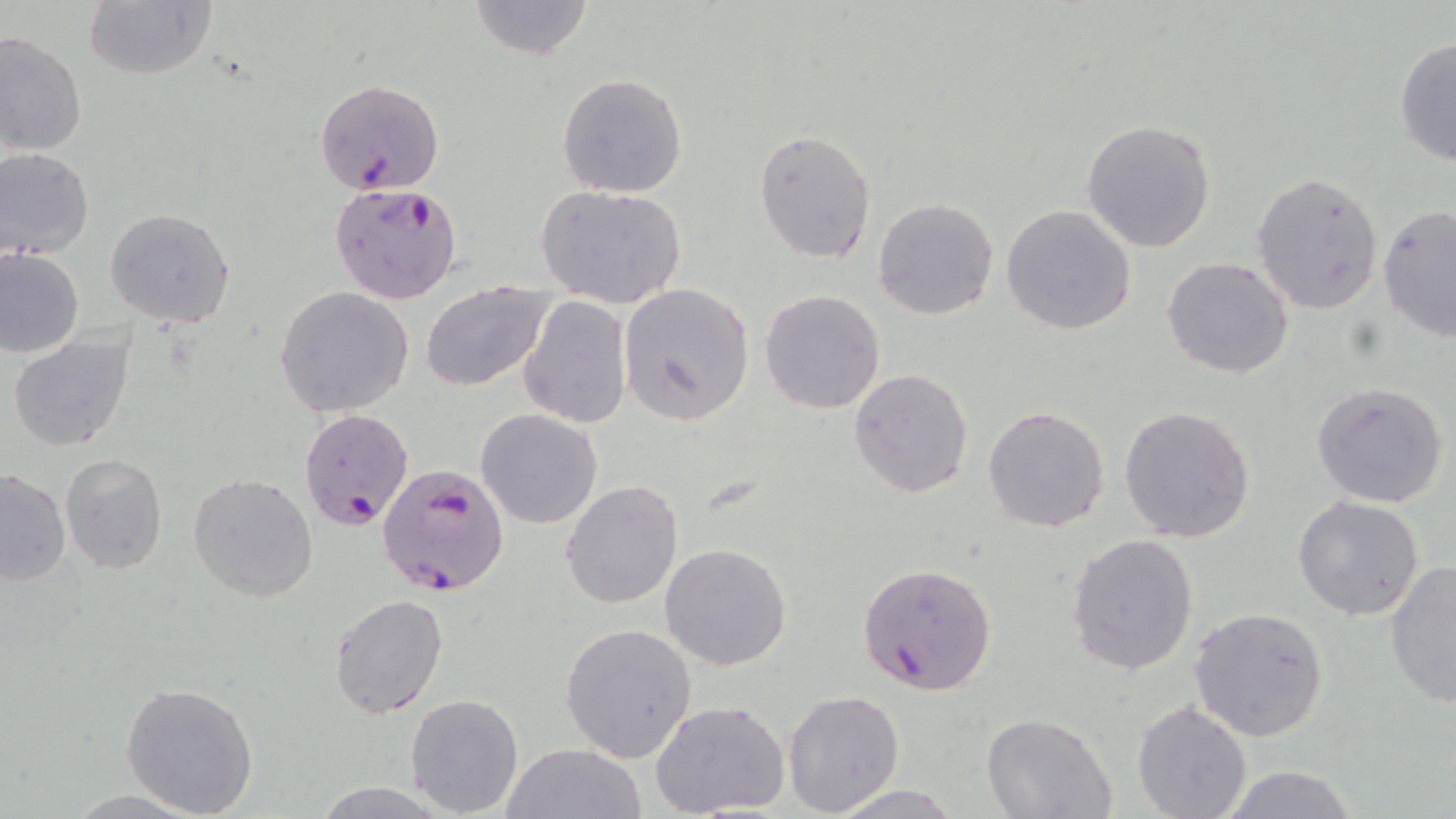
slide-level diagnosis = Plasmodium falciparum
modality = optical microscopy
magnification = 1000x
preparation = thin blood smear
image size = 1456×819 pixels
uninfected red blood cell locations = approximate bounding boxes as [x1, y1, x2, y2] in pixels: [82, 0, 216, 82], [466, 0, 592, 59], [0, 32, 86, 157], [1392, 38, 1456, 166], [556, 73, 688, 198], [1081, 119, 1220, 253], [754, 130, 877, 263], [0, 147, 95, 260], [1251, 170, 1385, 314], [535, 185, 687, 310], [872, 198, 1000, 320], [1000, 203, 1137, 335], [1377, 204, 1456, 342], [104, 208, 235, 329], [0, 249, 84, 359], [1161, 256, 1294, 378], [419, 280, 555, 392], [617, 282, 755, 426], [275, 287, 413, 417], [760, 289, 886, 415], [519, 294, 632, 429], [7, 333, 135, 454], [848, 367, 975, 500], [1311, 381, 1450, 507], [1119, 405, 1258, 543], [982, 406, 1111, 532], [476, 409, 603, 530], [60, 453, 169, 572], [0, 468, 72, 588], [187, 472, 319, 602], [562, 480, 683, 609], [1292, 495, 1425, 622], [1066, 532, 1199, 675], [659, 542, 792, 670], [1384, 560, 1456, 708], [329, 593, 449, 718], [1188, 607, 1330, 741], [560, 622, 697, 761], [121, 681, 260, 816], [783, 689, 905, 814], [405, 693, 525, 817], [648, 700, 792, 819], [1132, 700, 1254, 819], [980, 713, 1117, 819], [501, 742, 646, 819], [1212, 764, 1358, 819], [310, 781, 449, 817], [825, 784, 966, 817]
stain = May-Grünwald-Giemsa
field of view = single
Plasmodium falciparum-infected red blood cell locations = approximate bounding boxes as [x1, y1, x2, y2] in pixels: [314, 77, 444, 195], [329, 182, 462, 304], [299, 409, 417, 532], [378, 465, 508, 597], [857, 562, 999, 696]